Classify this cell by malaria status.
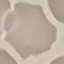
It is uninfected.

Summary:
  - Stain: Giemsa
  - Capture: smartphone through the microscope eyepiece
  - Image type: cell patch, automatically extracted from a larger field of view and resized to 64 × 64 pixels
  - Preparation: thin blood smear